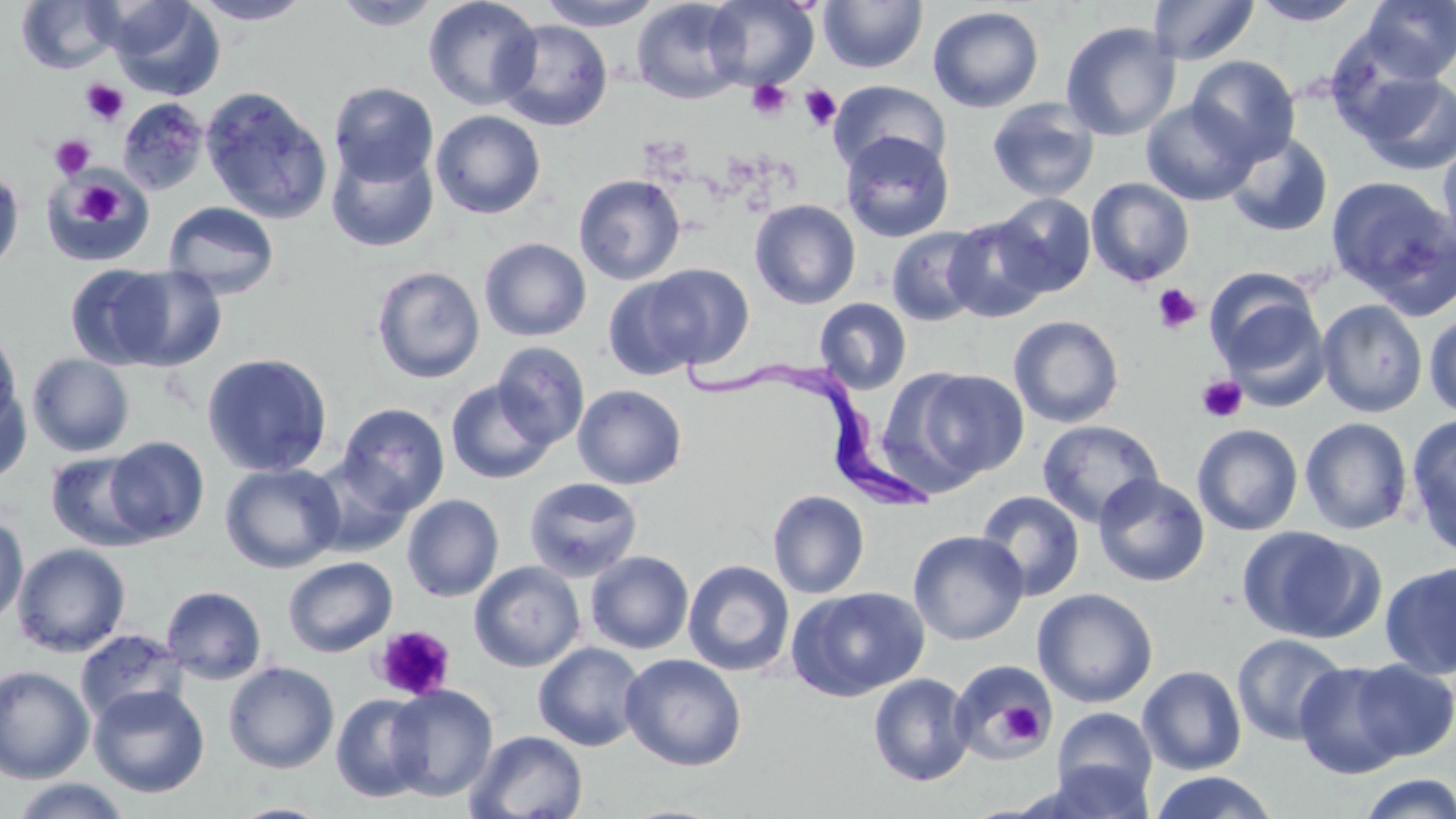
Summary:
  - Coordinate format: approximate bounding boxes as (x1,y1)-(x2,y2) corner pairs in pixels
  - Platelet locations: (81,78)-(128,126), (746,79)-(792,121), (800,84)-(841,130), (50,134)-(95,179), (73,181)-(124,227), (1153,283)-(1201,334), (1197,375)-(1247,424), (373,624)-(455,702), (998,701)-(1043,744)
  - Trypanosoma brucei locations: (684,348)-(937,515)
  - Uninfected red blood cell locations: (190,0)-(312,25), (423,0)-(543,110), (539,0)-(663,30), (631,0)-(747,104), (703,0)-(819,90), (1147,0)-(1259,65), (1250,0)-(1365,26), (1359,0)-(1456,83), (16,1)-(124,74), (109,1)-(223,100), (332,1)-(443,31), (818,1)-(928,73), (928,5)-(1045,113), (497,19)-(613,131), (1060,21)-(1181,141), (1186,55)-(1300,163), (1353,70)-(1456,176), (829,80)-(951,175), (328,81)-(438,186), (201,87)-(332,224), (116,97)-(210,196), (986,98)-(1100,202), (1141,99)-(1258,206), (430,110)-(546,219), (840,130)-(954,243), (1225,132)-(1333,237), (1438,140)-(1456,258), (327,145)-(438,253), (0,166)-(25,277), (42,173)-(151,265), (573,174)-(686,285), (1326,175)-(1455,310), (1086,178)-(1195,287), (992,192)-(1096,296), (749,199)-(861,309), (163,201)-(280,298), (944,216)-(1052,323), (886,226)-(989,326), (479,238)-(591,341), (64,264)-(176,369), (643,264)-(753,370), (371,265)-(485,383), (109,267)-(227,372), (1205,267)-(1322,376), (602,275)-(706,381), (814,297)-(912,394), (1316,299)-(1428,418), (1423,309)-(1456,418), (1008,315)-(1125,428), (0,324)-(24,433), (491,341)-(591,448), (201,352)-(333,477), (27,353)-(135,457), (910,368)-(1029,482), (445,379)-(557,484), (0,382)-(33,485), (572,384)-(687,490), (337,403)-(450,515), (1405,414)-(1456,556), (1300,416)-(1414,535), (1036,419)-(1163,527), (1192,424)-(1304,536), (103,437)-(210,543), (45,452)-(154,551), (307,459)-(413,557), (220,462)-(345,573), (1093,474)-(1210,587), (524,477)-(643,581), (767,490)-(870,599), (975,490)-(1086,602), (402,494)-(505,602), (0,514)-(28,628), (1238,526)-(1379,643), (908,529)-(1029,645), (12,543)-(131,656), (585,551)-(694,654), (282,556)-(397,657), (683,560)-(795,677), (1379,560)-(1456,680), (469,561)-(586,672), (161,585)-(267,685), (787,586)-(930,702), (1032,588)-(1158,708), (75,628)-(188,725), (1231,632)-(1349,745), (533,642)-(647,752), (620,653)-(747,771), (949,659)-(1056,766), (1348,659)-(1456,761), (223,661)-(339,774), (1294,661)-(1409,779), (1137,664)-(1247,776), (0,665)-(96,784), (868,673)-(975,787), (88,683)-(210,798), (385,684)-(498,801), (330,693)-(433,802), (1052,707)-(1158,806), (465,729)-(589,819), (1040,760)-(1156,818), (1151,770)-(1277,819), (1355,773)-(1456,819), (8,778)-(133,818), (230,802)-(335,819)
  - Slide-level diagnosis: Trypanosoma brucei
  - Preparation: thin blood film
  - Image size: 1456×819 pixels
  - Modality: light microscopy
  - Stain: May-Grünwald-Giemsa
  - Magnification: 1000x
  - Field of view: single